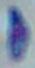
{
  "identification": "Toxoplasma gondii",
  "magnification": "1000x",
  "modality": "micrograph"
}